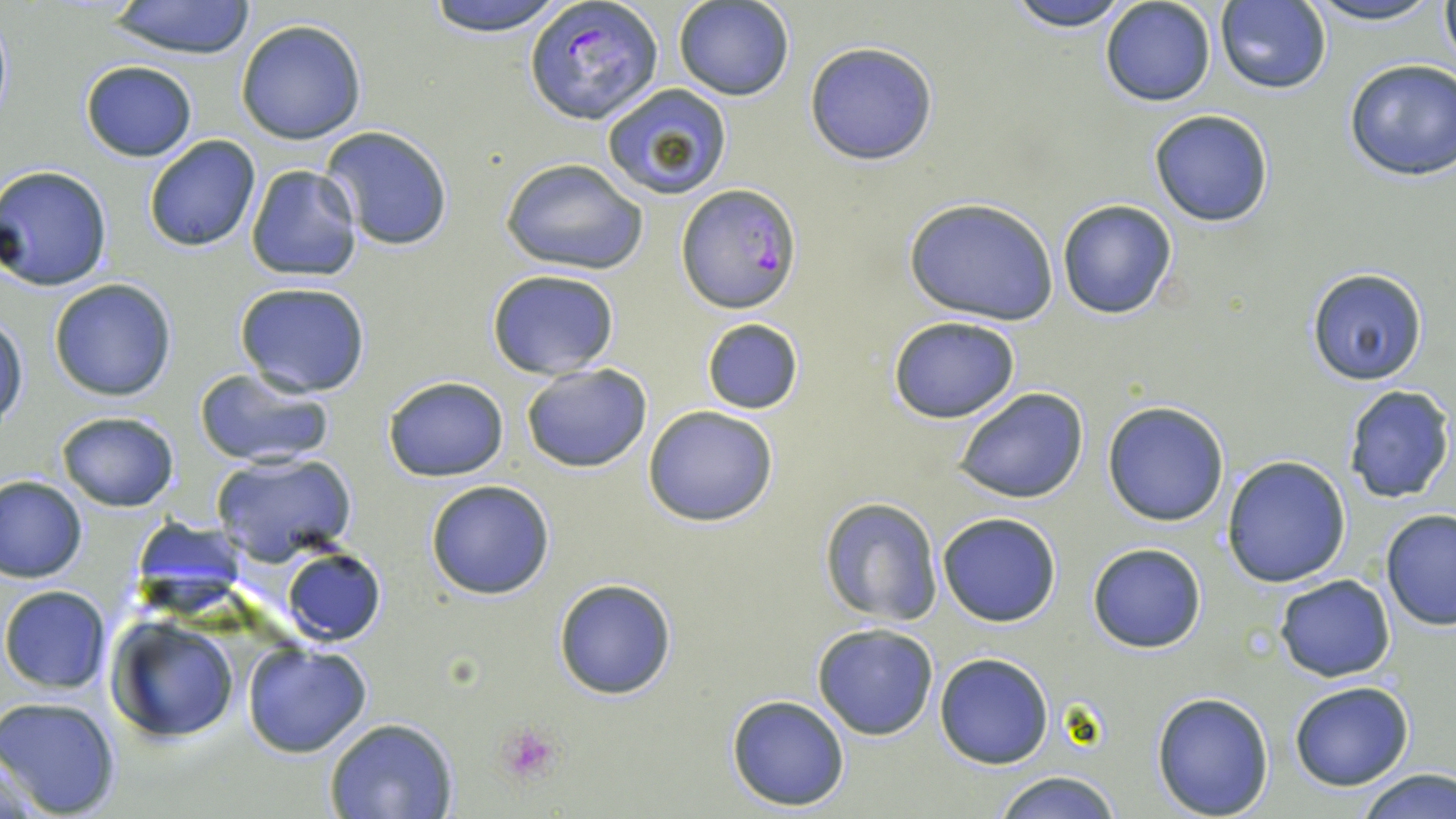
Summary:
  - Coordinate format: approximate bounding boxes as (x1, y1, x2, y2) in pixels
  - Platelet locations: (494, 723, 565, 786)
  - Uninfected red blood cell locations: (421, 0, 571, 36), (1002, 0, 1138, 31), (1100, 0, 1217, 107), (1297, 0, 1448, 27), (1437, 0, 1456, 71), (104, 1, 259, 60), (675, 1, 796, 102), (1214, 2, 1332, 94), (235, 18, 368, 144), (805, 41, 939, 164), (1344, 58, 1456, 180), (80, 61, 197, 162), (601, 83, 733, 199), (1148, 109, 1275, 227), (320, 126, 454, 251), (144, 134, 261, 251), (499, 157, 651, 276), (2, 165, 113, 291), (244, 166, 363, 282), (902, 197, 1060, 325), (1057, 200, 1178, 320), (486, 269, 620, 380), (1307, 269, 1429, 386), (48, 278, 180, 403), (233, 280, 371, 397), (0, 312, 29, 429), (887, 316, 1020, 423), (699, 317, 805, 415), (520, 361, 654, 474), (191, 368, 337, 469), (383, 375, 509, 480), (1342, 385, 1454, 503), (952, 386, 1089, 504), (1102, 401, 1230, 526), (643, 404, 779, 527), (55, 411, 180, 511), (210, 451, 356, 566), (1222, 455, 1352, 588), (1, 475, 87, 583), (425, 479, 556, 600), (819, 497, 943, 626), (1380, 508, 1456, 630), (936, 511, 1063, 627), (131, 517, 250, 615), (1087, 542, 1208, 653), (282, 547, 385, 645), (1274, 574, 1396, 683), (552, 577, 679, 701), (0, 586, 114, 696), (107, 616, 241, 741), (811, 622, 939, 741), (242, 641, 373, 758), (933, 652, 1054, 769), (1288, 681, 1414, 791), (1151, 690, 1274, 817), (726, 694, 851, 810), (0, 696, 123, 818), (324, 718, 459, 818), (1355, 768, 1455, 819), (993, 769, 1121, 819)
  - Plasmodium falciparum-infected red blood cell locations: (525, 1, 662, 126), (677, 185, 803, 313)
  - Slide-level diagnosis: Plasmodium falciparum
  - Preparation: thin blood smear
  - Magnification: 1000x
  - Field of view: single
  - Image size: 1456×819 pixels
  - Stain: May-Grünwald-Giemsa
  - Modality: light microscopy